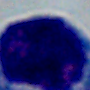 A white blood cell is seen. 1000x magnification. Micrograph.